Assess this cell for malaria.
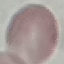
It is uninfected.

Photographed with a smartphone camera at the microscope eyepiece. Cell patch, automatically extracted from a larger field of view and resized to 64 × 64 pixels. Thin blood film. Giemsa-stained preparation.